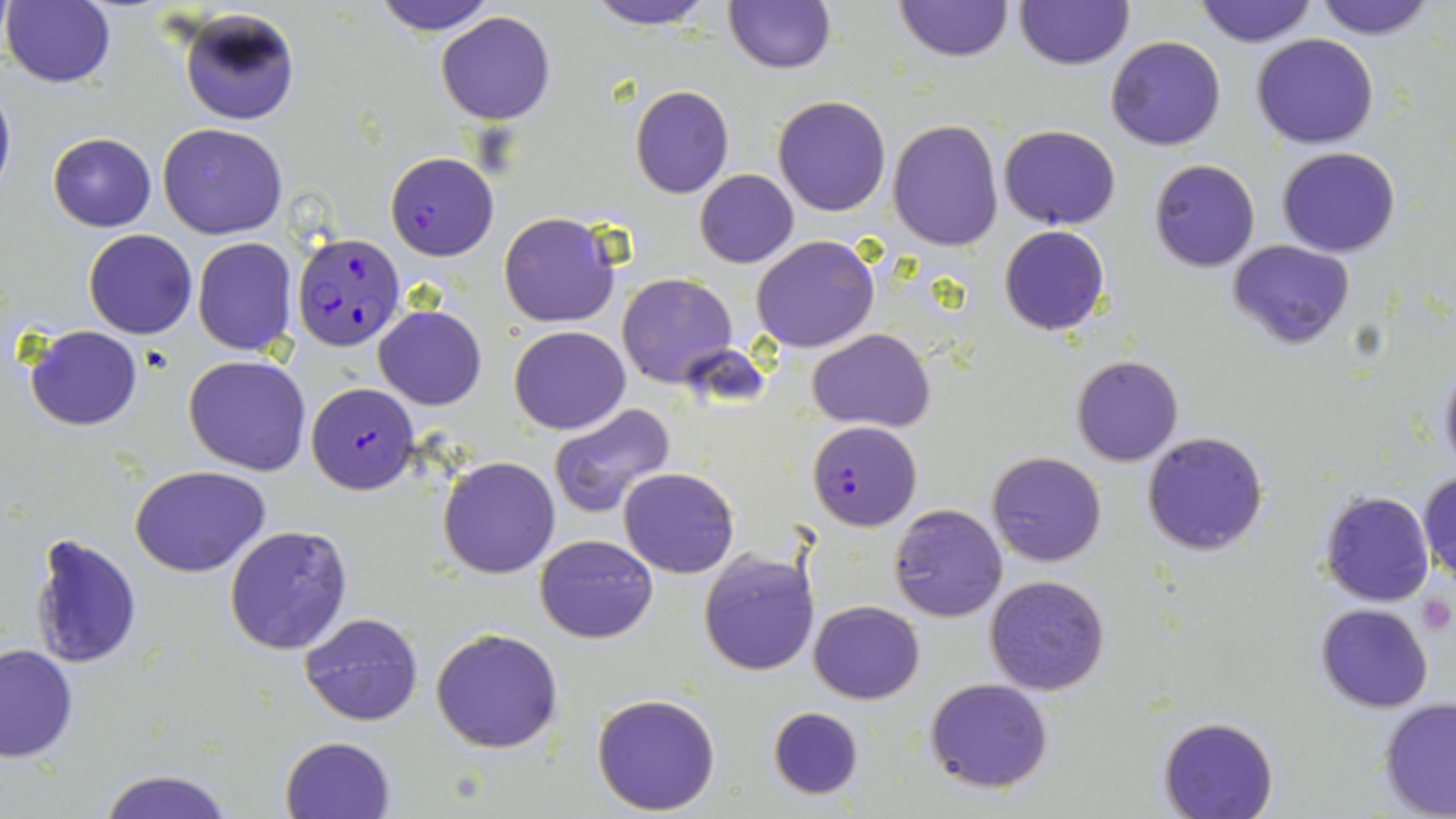

Summary:
  - Coordinate format: approximate bounding boxes as (x1,y1)-(x2,y2) corner pairs in pixels
  - Platelet locations: (1417,595)-(1452,632)
  - Plasmodium falciparum-infected red blood cell locations: (385,151)-(499,260), (293,229)-(403,350), (306,383)-(419,495), (807,421)-(921,530)
  - Uninfected red blood cell locations: (373,0)-(498,34), (581,0)-(718,29), (891,0)-(1016,63), (1194,0)-(1316,46), (1312,0)-(1437,40), (2,1)-(116,88), (1015,1)-(1131,70), (723,2)-(836,74), (177,8)-(299,126), (436,12)-(555,125), (1252,33)-(1379,149), (1105,37)-(1226,151), (0,75)-(16,202), (629,85)-(735,199), (772,96)-(892,217), (888,119)-(1003,251), (158,123)-(289,240), (999,124)-(1121,230), (47,132)-(156,232), (1276,146)-(1401,257), (1149,159)-(1260,272), (694,169)-(799,268), (498,210)-(620,327), (999,225)-(1109,337), (83,229)-(197,339), (753,234)-(878,352), (192,237)-(297,356), (1228,239)-(1355,350), (618,273)-(739,389), (374,305)-(487,410), (24,324)-(143,431), (509,325)-(630,434), (809,328)-(933,430), (184,355)-(311,476), (1072,356)-(1184,465), (1437,359)-(1456,476), (548,402)-(678,519), (1142,430)-(1269,557), (986,450)-(1107,567), (438,456)-(561,579), (130,464)-(272,576), (619,467)-(738,578), (1417,472)-(1456,580), (1318,491)-(1435,608), (888,504)-(1007,622), (223,523)-(353,655), (27,531)-(144,668), (534,533)-(658,643), (697,549)-(819,677), (983,574)-(1110,696), (1415,588)-(1453,639), (809,600)-(925,704), (1315,603)-(1435,714), (298,611)-(423,727), (431,626)-(563,752), (0,642)-(78,763), (924,678)-(1055,792), (590,692)-(721,815), (1379,699)-(1456,817), (767,706)-(865,801), (1158,716)-(1280,819), (279,735)-(398,819), (96,767)-(235,819)
  - Slide-level diagnosis: Plasmodium falciparum
  - Preparation: thin blood film
  - Magnification: 1000x
  - Modality: optical microscopy
  - Stain: May-Grünwald-Giemsa
  - Field of view: one of a larger specimen
  - Image size: 1456×819 pixels